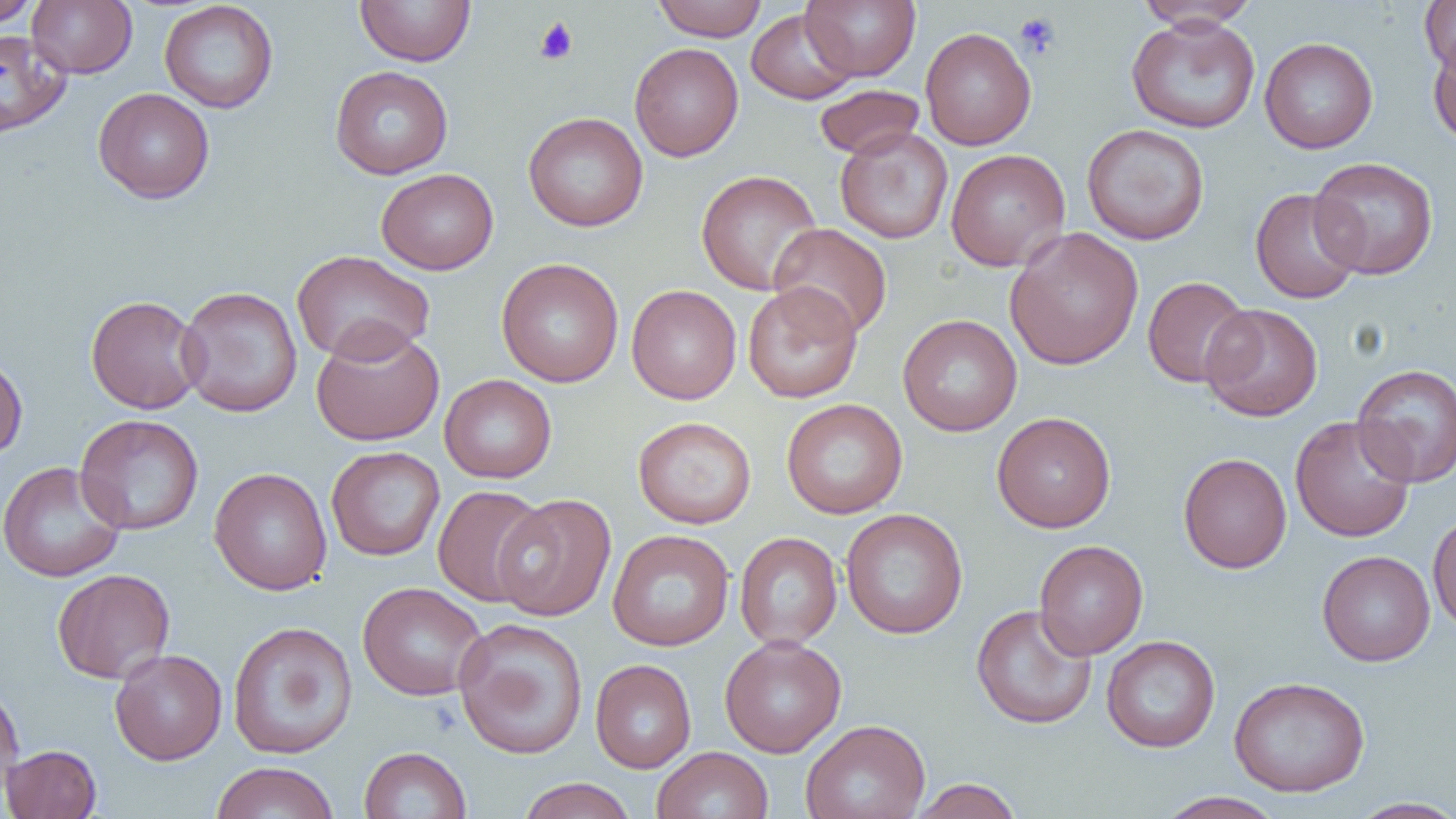

slide_level_diagnosis: no evidence of blood parasites
platelet_locations: 'approximate bounding boxes as named x1/y1/x2/y2 corners in pixels: (x1=1013, y1=11, x2=1062, y2=59), (x1=533, y1=17, x2=579, y2=65)'
magnification: 1000x
image_size: 1456×819 pixels
field_of_view: single
uninfected_red_blood_cell_locations: 'approximate bounding boxes as named x1/y1/x2/y2 corners in pixels: (x1=0, y1=0, x2=41, y2=28), (x1=27, y1=0, x2=137, y2=78), (x1=355, y1=0, x2=476, y2=66), (x1=652, y1=0, x2=768, y2=41), (x1=801, y1=0, x2=920, y2=82), (x1=1419, y1=0, x2=1456, y2=74), (x1=159, y1=1, x2=278, y2=113), (x1=1135, y1=2, x2=1260, y2=32), (x1=746, y1=8, x2=859, y2=104), (x1=1125, y1=15, x2=1260, y2=133), (x1=920, y1=27, x2=1036, y2=150), (x1=0, y1=29, x2=71, y2=137), (x1=1427, y1=32, x2=1456, y2=147), (x1=1259, y1=37, x2=1378, y2=153), (x1=629, y1=43, x2=744, y2=161), (x1=330, y1=65, x2=453, y2=179), (x1=813, y1=84, x2=925, y2=160), (x1=93, y1=87, x2=215, y2=204), (x1=523, y1=112, x2=648, y2=232), (x1=1082, y1=123, x2=1210, y2=245), (x1=835, y1=126, x2=953, y2=244), (x1=945, y1=148, x2=1071, y2=271), (x1=1309, y1=156, x2=1439, y2=280), (x1=376, y1=168, x2=499, y2=275), (x1=695, y1=169, x2=823, y2=295), (x1=1251, y1=188, x2=1363, y2=304), (x1=768, y1=223, x2=893, y2=339), (x1=1005, y1=226, x2=1144, y2=371), (x1=291, y1=250, x2=435, y2=364), (x1=496, y1=258, x2=624, y2=387), (x1=1142, y1=276, x2=1254, y2=388), (x1=743, y1=282, x2=863, y2=403), (x1=626, y1=284, x2=742, y2=405), (x1=176, y1=285, x2=303, y2=417), (x1=85, y1=295, x2=205, y2=414), (x1=1201, y1=304, x2=1323, y2=421), (x1=897, y1=314, x2=1022, y2=436), (x1=310, y1=323, x2=445, y2=447), (x1=0, y1=352, x2=28, y2=460), (x1=1351, y1=363, x2=1456, y2=487), (x1=439, y1=374, x2=556, y2=483), (x1=781, y1=398, x2=908, y2=519), (x1=992, y1=411, x2=1116, y2=533), (x1=74, y1=414, x2=204, y2=535), (x1=1290, y1=415, x2=1417, y2=542), (x1=633, y1=416, x2=757, y2=529), (x1=326, y1=446, x2=445, y2=561), (x1=1178, y1=452, x2=1292, y2=573), (x1=0, y1=461, x2=126, y2=582), (x1=209, y1=467, x2=332, y2=595), (x1=433, y1=485, x2=549, y2=607), (x1=492, y1=493, x2=617, y2=621), (x1=840, y1=508, x2=968, y2=639), (x1=1428, y1=509, x2=1456, y2=635), (x1=492, y1=516, x2=734, y2=635), (x1=608, y1=529, x2=734, y2=651), (x1=734, y1=532, x2=842, y2=649), (x1=1033, y1=539, x2=1148, y2=659), (x1=1317, y1=550, x2=1435, y2=666), (x1=51, y1=568, x2=175, y2=684), (x1=357, y1=581, x2=488, y2=701), (x1=971, y1=603, x2=1098, y2=729), (x1=453, y1=617, x2=589, y2=760), (x1=228, y1=620, x2=357, y2=759), (x1=719, y1=635, x2=847, y2=758), (x1=1101, y1=635, x2=1220, y2=752), (x1=109, y1=649, x2=227, y2=765), (x1=590, y1=659, x2=696, y2=773), (x1=1228, y1=676, x2=1371, y2=796), (x1=0, y1=682, x2=25, y2=802), (x1=800, y1=718, x2=930, y2=819), (x1=2, y1=744, x2=102, y2=818), (x1=359, y1=746, x2=472, y2=819), (x1=651, y1=747, x2=774, y2=819), (x1=210, y1=761, x2=340, y2=819), (x1=517, y1=777, x2=637, y2=819), (x1=907, y1=778, x2=1024, y2=818), (x1=1156, y1=791, x2=1286, y2=819), (x1=1347, y1=796, x2=1456, y2=818)'
modality: light microscopy
preparation: thin blood smear